Identify the parasite.
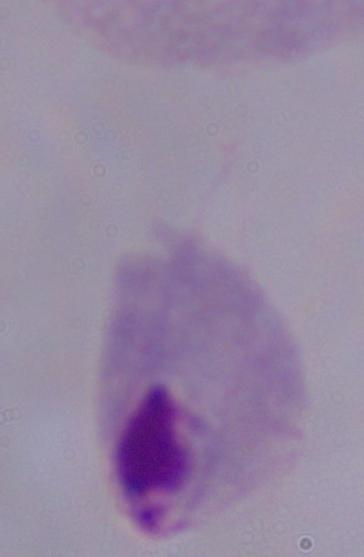

A trichomonad.

{
  "modality": "micrograph",
  "magnification": "1000x"
}